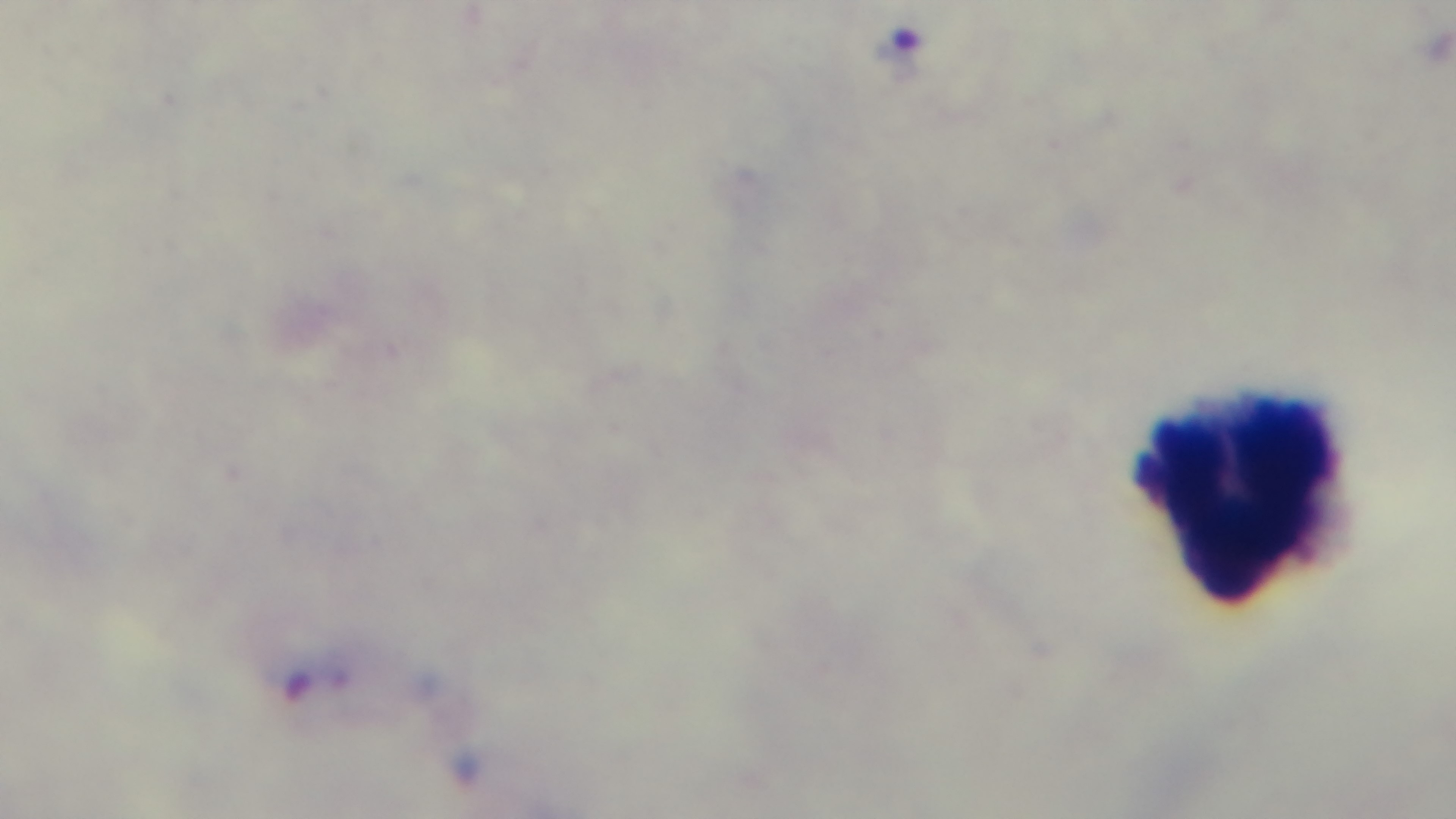
Summary:
  - Malaria status: positive
  - Capture: mounted 4K digital camera
  - Stain: Giemsa
  - Preparation: thick blood film
  - Field of view: single
  - Modality: light microscopy
  - Objective: 100x oil immersion